Name the parasite shown.
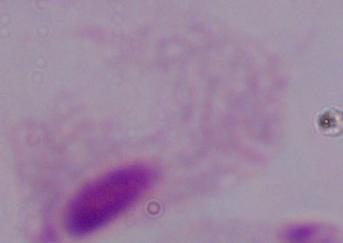
This is a trichomonad.

modality = photomicrograph
magnification = 1000x